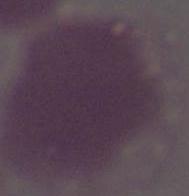
magnification = 1000x
modality = photomicrograph
identification = erythrocyte